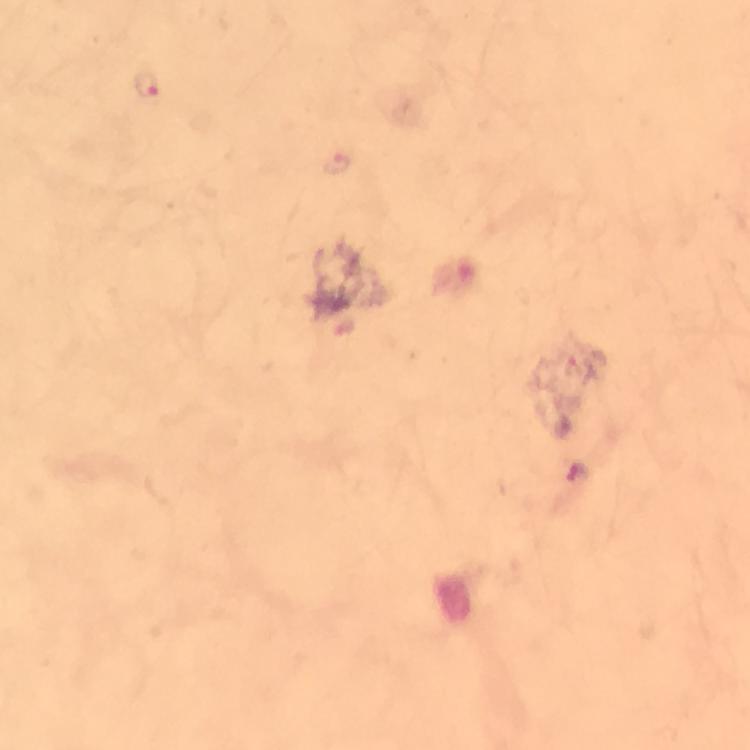

magnification = 100x
cropped from = one field of view
capture = smartphone mounted on the microscope
immersion oil = applied
context = from a malaria diagnostic workup
preparation = thick blood film
image size = 750×750 pixels
stain = Giemsa
Plasmodium parasite locations = approximate centers as {x, y} in pixels: {146, 84}, {336, 164}